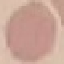

Summary:
  - Result: no malaria parasites detected
  - Image type: automatically extracted cell patch, resized to 64 × 64 pixels
  - Preparation: thin blood film
  - Capture: smartphone through the microscope eyepiece
  - Stain: Giemsa